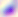

{
  "identification": "Toxoplasma gondii",
  "magnification": "400x",
  "modality": "micrograph"
}